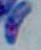
Summary:
  - Identification: Toxoplasma gondii
  - Modality: photomicrograph
  - Magnification: 1000x